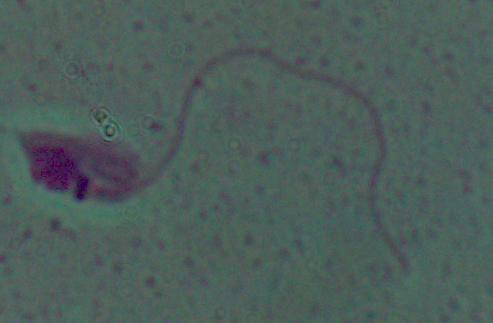 Micrograph. A Leishmania parasite is seen. Captured at 1000x magnification.